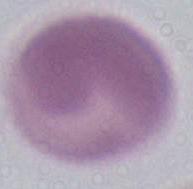

Photomicrograph. An erythrocyte is seen. Captured at 1000x magnification.